Name the parasite shown.
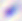

This is Toxoplasma gondii.

{
  "modality": "micrograph",
  "magnification": "400x"
}